Comment on the morphology of the red blood cells.
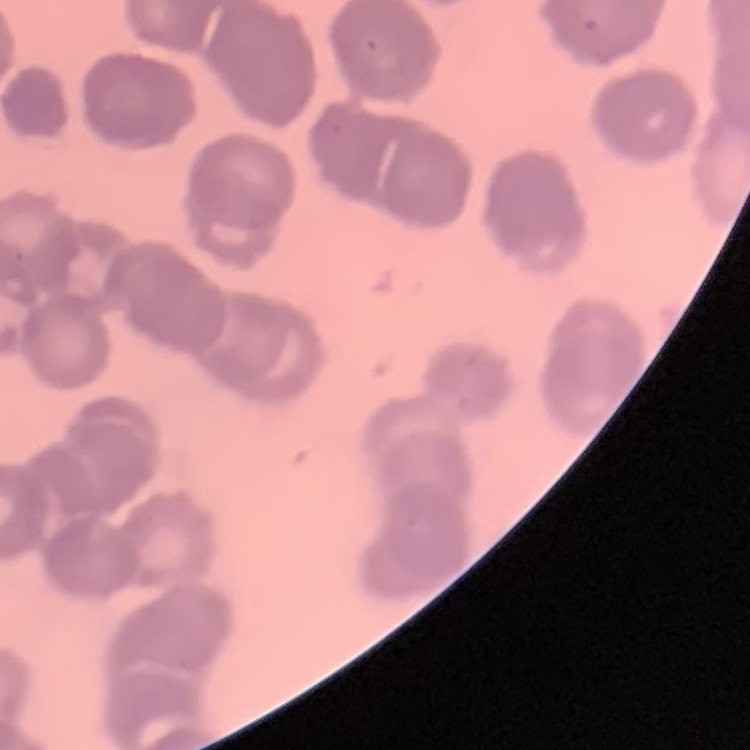
Rouleaux formation.

preparation: thin blood smear
image_type: one tile cut from a larger photomicrograph
stain: Field's or Giemsa